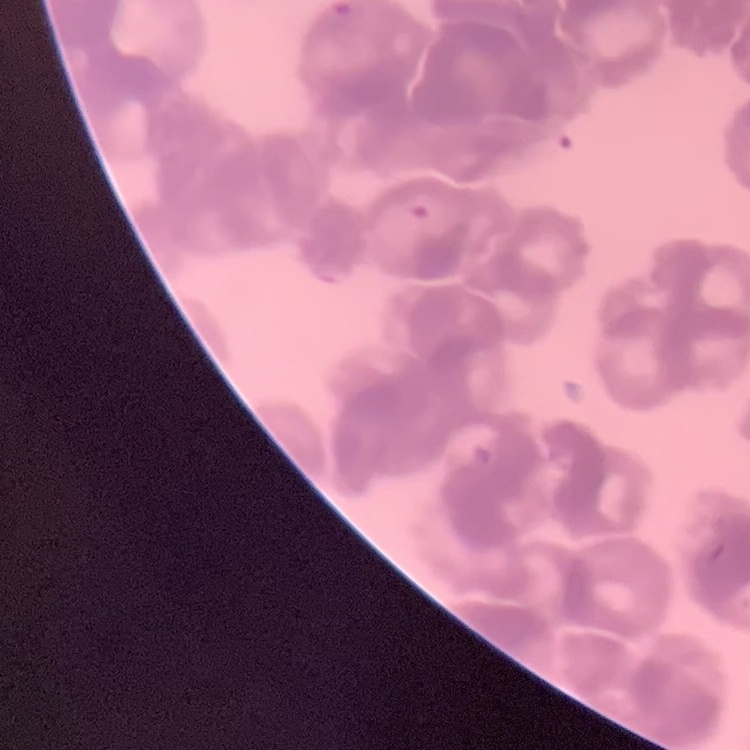

erythrocyte_morphology: rouleaux formation
preparation: thin blood smear
image_type: one tile cut from a larger photomicrograph
stain: Field's or Giemsa